Name the cell type shown.
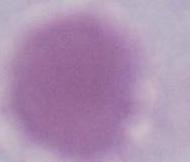
An erythrocyte.

Captured at 1000x magnification. Micrograph.